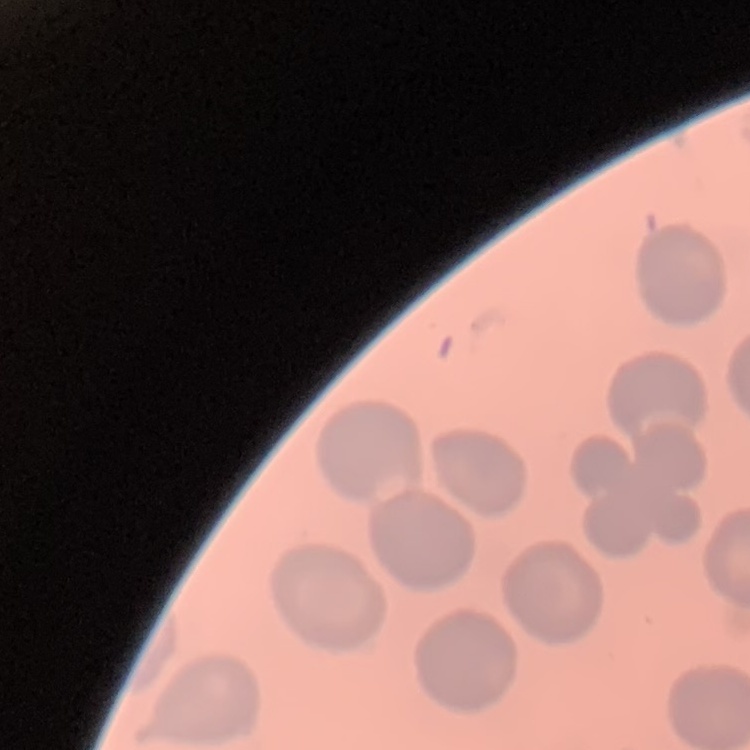

The erythrocytes show no rouleaux formation. Stained with either Field's or Giemsa. One tile cut from a larger photomicrograph. Thin blood smear.